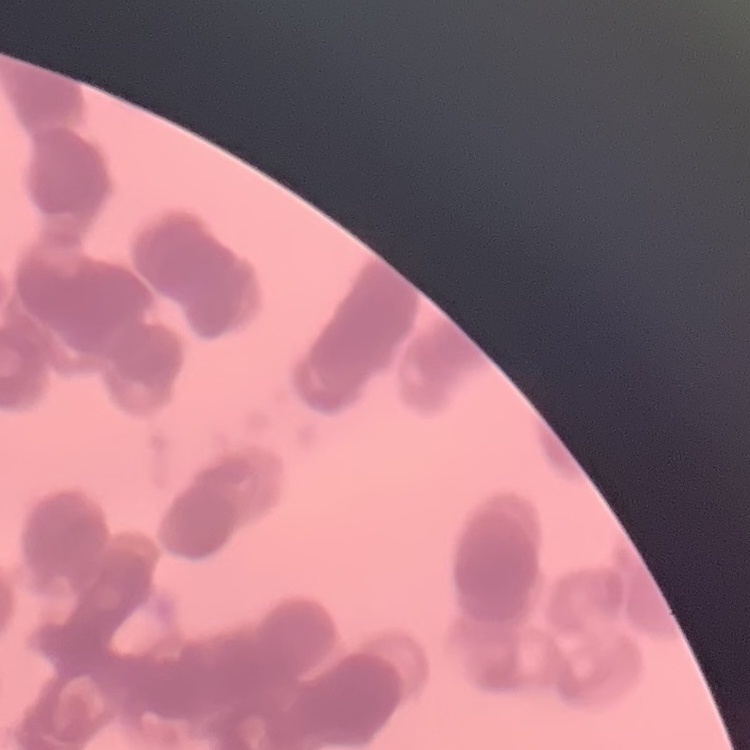

red_blood_cell_morphology: rouleaux formation
stain: Field's or Giemsa
image_type: square crop of a larger photomicrograph
preparation: thin blood smear